State which parasite is depicted.
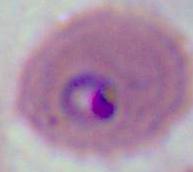
This is Plasmodium.

400x or 1000x magnification. Photomicrograph.